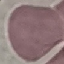 Result: no malaria parasites seen. Thin smear of blood. Acquired by smartphone through the microscope eyepiece. Automatically extracted cell patch, resized to 64 × 64 pixels. Giemsa-stained preparation.